Describe the morphology of the erythrocytes.
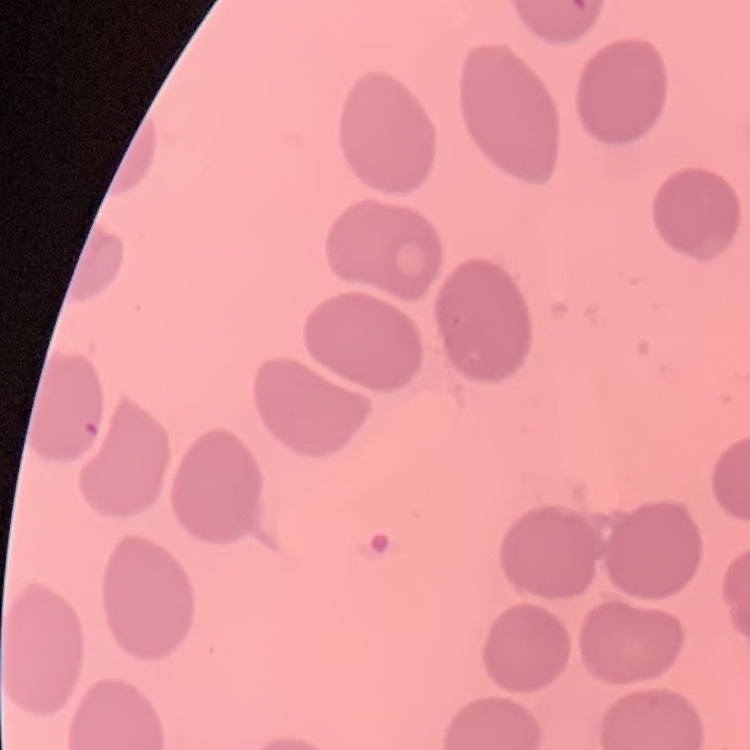
They show no rouleaux formation.

image type = square crop of a larger photomicrograph
stain = Field's or Giemsa
preparation = thin peripheral smear